Assess this cell for malaria.
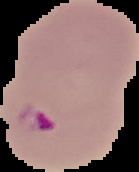
It is parasitized.

Image is 139×172 pixels. From a thin blood smear. The area outside the segmented cell region is set to black.